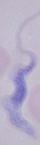 Captured at 1000x magnification. A trypanosome is shown. Photomicrograph.